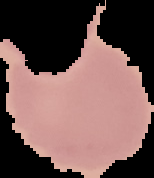

result = no Plasmodium parasites seen
preparation = thin blood film
image type = segmented cell region with the area outside set to black
image size = 154×178 pixels